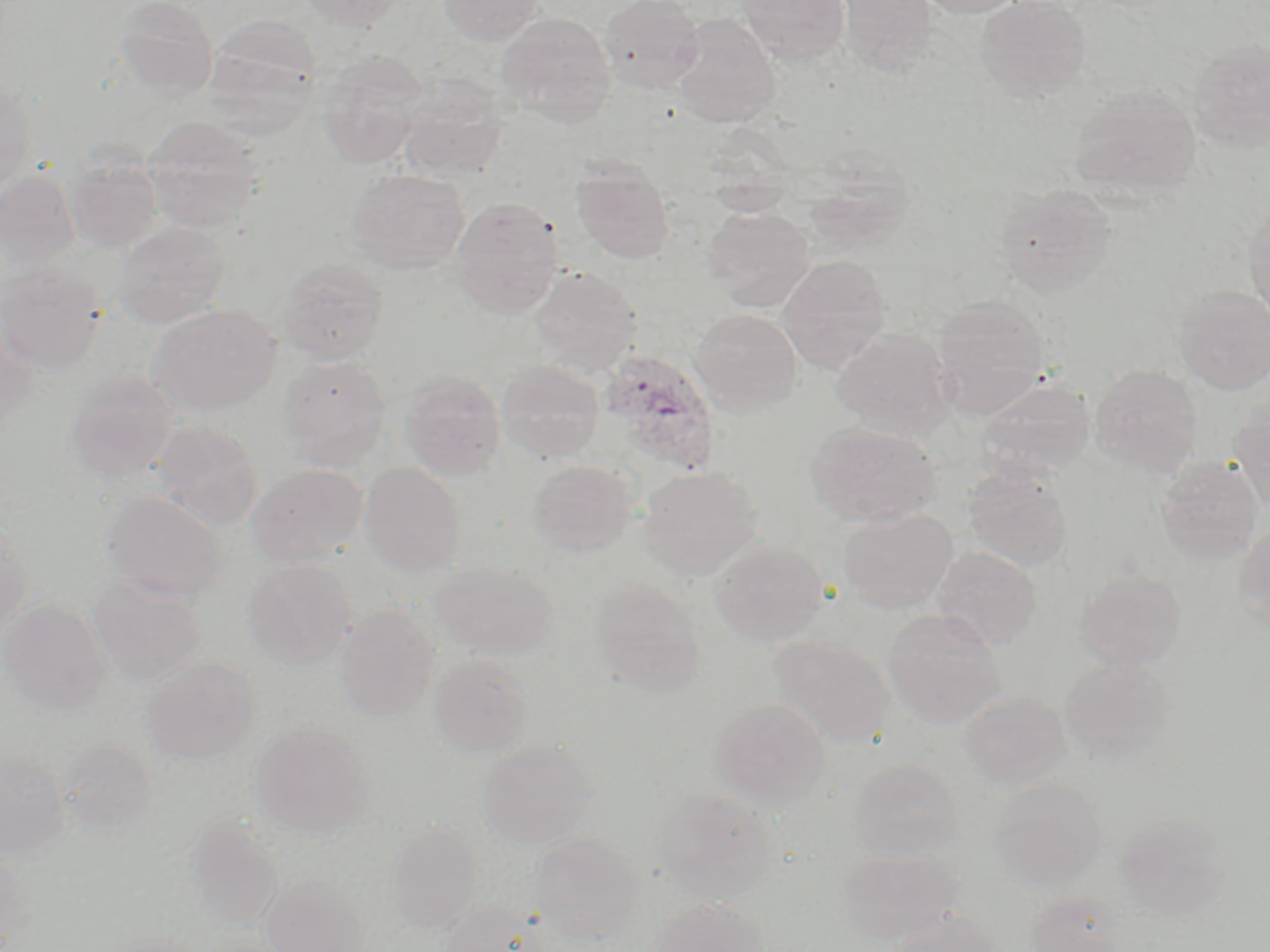

Summary:
  - Coordinate format: approximate bounding boxes as (x1, y1, x2, y2) in pixels
  - Uninfected red blood cell locations: (113, 0, 219, 100), (299, 0, 407, 30), (439, 0, 545, 45), (600, 0, 704, 92), (740, 0, 850, 65), (837, 0, 936, 74), (917, 0, 1025, 17), (976, 0, 1090, 101), (496, 11, 616, 125), (671, 15, 780, 127), (203, 16, 322, 139), (1188, 39, 1270, 154), (317, 51, 428, 168), (398, 76, 510, 183), (0, 81, 35, 197), (1068, 84, 1202, 201), (144, 116, 265, 232), (65, 155, 163, 254), (572, 160, 674, 263), (802, 160, 914, 254), (347, 169, 469, 275), (0, 171, 81, 271), (995, 185, 1116, 297), (450, 197, 563, 318), (1244, 200, 1270, 326), (705, 207, 814, 311), (115, 221, 231, 326), (779, 255, 891, 374), (277, 257, 389, 365), (0, 263, 106, 374), (529, 266, 643, 373), (1174, 285, 1270, 395), (933, 293, 1051, 413), (149, 305, 280, 415), (690, 309, 801, 413), (0, 323, 39, 438), (832, 328, 955, 438), (280, 355, 392, 470), (496, 360, 604, 463), (1090, 364, 1203, 476), (401, 370, 506, 478), (65, 372, 179, 485), (978, 377, 1096, 475), (1230, 404, 1270, 514), (153, 418, 264, 530), (805, 421, 941, 527), (1155, 457, 1263, 564), (527, 460, 639, 557), (360, 463, 467, 576), (247, 464, 369, 568), (962, 464, 1073, 571), (639, 466, 761, 580), (102, 490, 229, 604), (839, 509, 957, 612), (1233, 523, 1270, 635), (0, 525, 33, 640), (710, 539, 830, 645), (932, 546, 1041, 650), (243, 559, 358, 669), (429, 561, 556, 657), (1075, 569, 1186, 672), (89, 576, 207, 685), (590, 577, 708, 700), (1, 598, 112, 713), (334, 604, 440, 721), (883, 608, 1006, 727), (770, 633, 894, 746), (427, 655, 534, 759), (141, 657, 261, 766), (1060, 658, 1175, 762), (959, 691, 1071, 789), (711, 698, 830, 807), (251, 721, 375, 837), (478, 739, 598, 850), (0, 750, 71, 858), (849, 758, 964, 862), (990, 776, 1108, 889), (650, 788, 776, 902), (1113, 812, 1231, 919), (186, 819, 284, 928), (385, 824, 482, 932), (528, 832, 643, 942), (0, 845, 29, 948), (840, 849, 963, 945), (260, 873, 370, 952), (1020, 890, 1129, 952), (648, 898, 770, 952), (440, 901, 549, 952), (880, 910, 1006, 952)
  - Plasmodium ovale-infected red blood cell locations: (601, 349, 722, 475)
  - Slide-level diagnosis: Plasmodium ovale
  - Modality: light microscopy
  - Magnification: 1000x
  - Stain: May-Grünwald-Giemsa
  - Preparation: thin blood smear
  - Image size: 1270×952 pixels
  - Field of view: one of a larger specimen